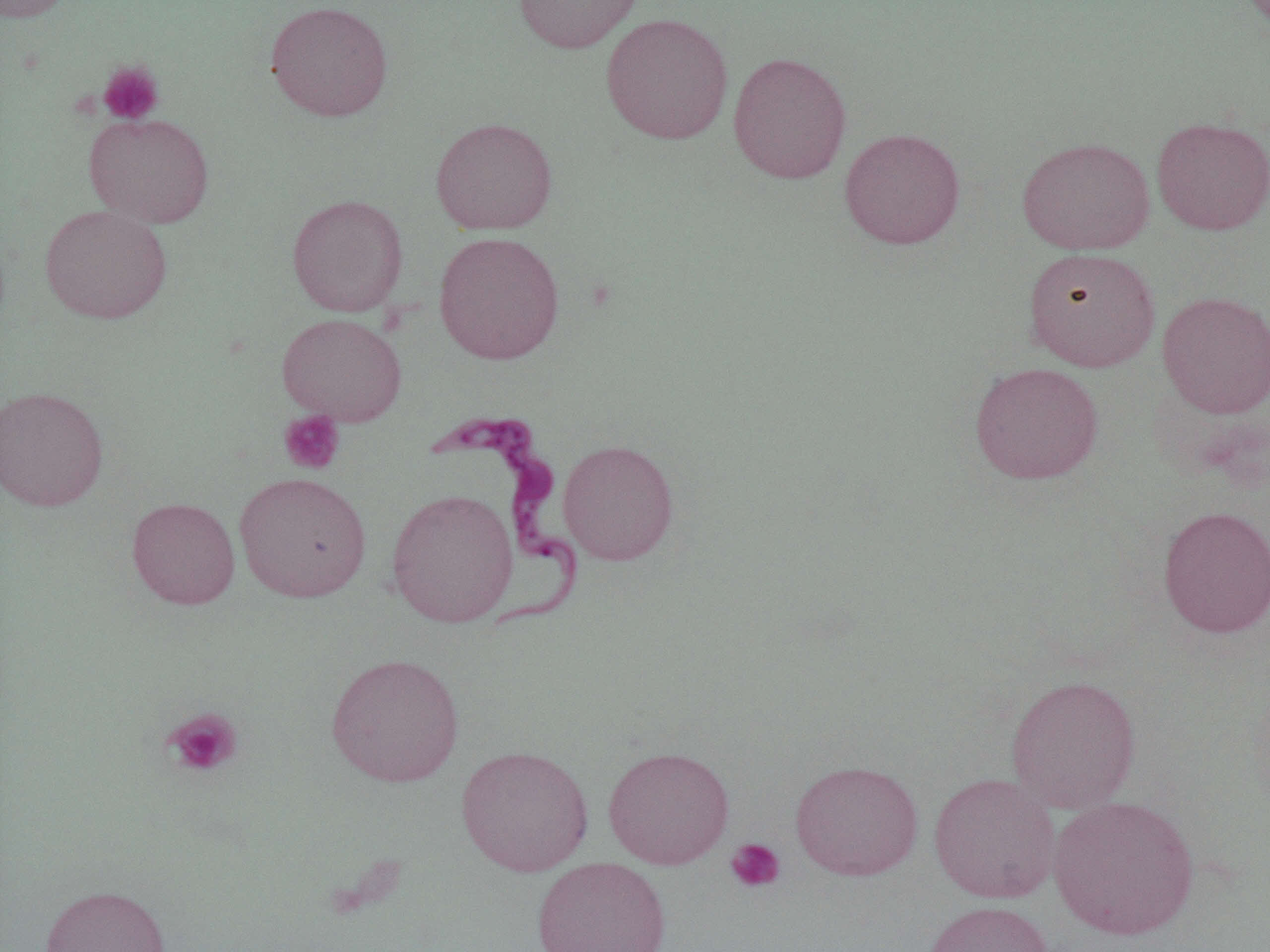

Summary:
  - Coordinate format: approximate bounding boxes as [x1, y1, x2, y2] in pixels
  - Trypanosoma brucei locations: [425, 412, 585, 633]
  - Uninfected red blood cell locations: [0, 0, 74, 22], [513, 0, 644, 54], [265, 1, 393, 122], [600, 12, 733, 145], [727, 51, 852, 184], [83, 112, 215, 228], [430, 117, 558, 235], [1151, 117, 1270, 235], [839, 127, 966, 250], [1016, 136, 1155, 255], [286, 194, 408, 317], [39, 204, 172, 324], [433, 231, 565, 365], [1023, 246, 1160, 371], [1157, 291, 1270, 418], [276, 313, 407, 425], [969, 362, 1104, 484], [0, 385, 109, 511], [557, 439, 680, 565], [234, 472, 371, 602], [387, 488, 519, 626], [127, 497, 240, 609], [1157, 505, 1270, 638], [325, 652, 464, 787], [1005, 674, 1142, 812], [456, 744, 593, 876], [603, 745, 734, 869], [790, 760, 923, 880], [929, 772, 1060, 904], [1049, 796, 1200, 940], [531, 857, 671, 951], [39, 884, 171, 951], [922, 901, 1054, 952]
  - Platelet locations: [98, 60, 165, 125], [279, 410, 344, 475], [162, 707, 243, 778], [725, 837, 785, 893]
  - Slide-level diagnosis: Trypanosoma brucei
  - Preparation: thin blood film
  - Image size: 1270×952 pixels
  - Modality: light microscopy
  - Magnification: 1000x
  - Field of view: single